State which parasite is depicted.
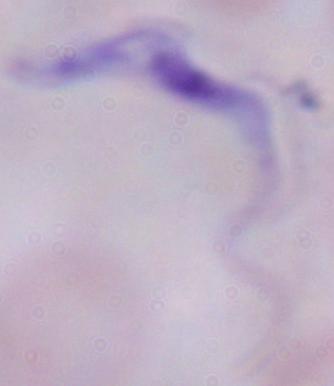

This is a trypanosome.

modality: micrograph
magnification: 1000x